State which parasite is depicted.
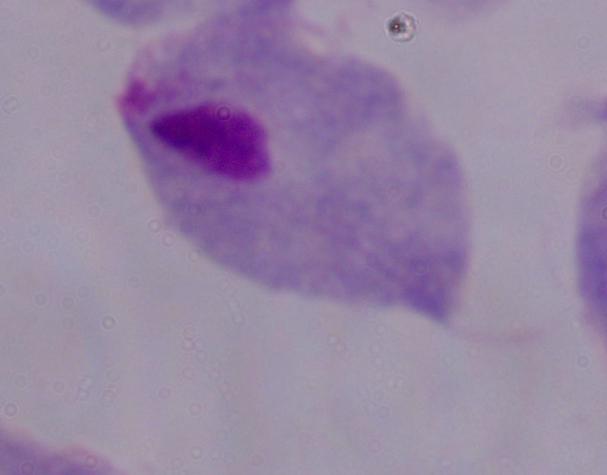
This is a trichomonad.

Micrograph. Captured at 1000x magnification.